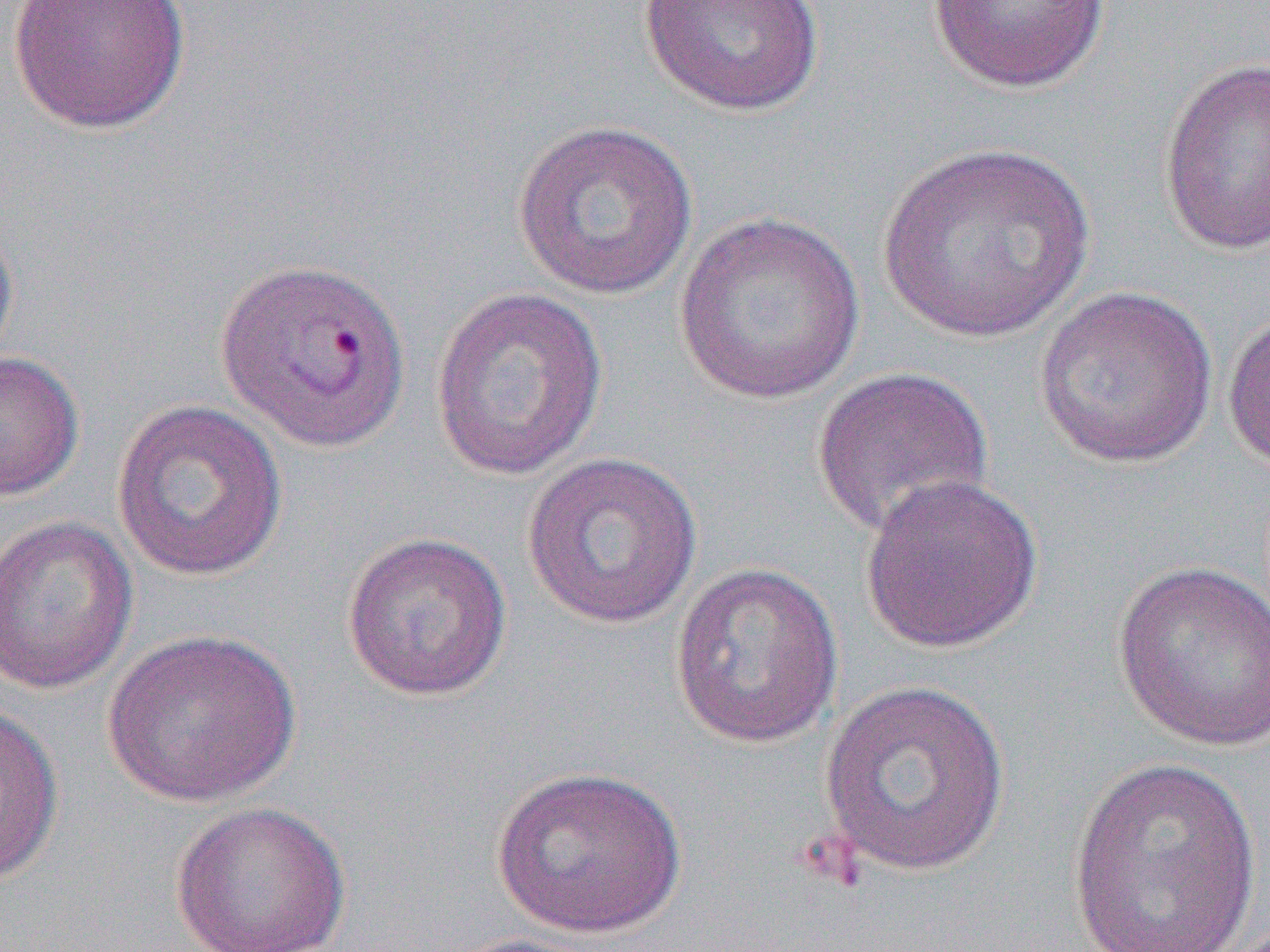

slide-level diagnosis = Plasmodium vivax
modality = light microscopy
magnification = 1000x
field of view = single
uninfected red blood cell locations = approximate bounding boxes as (x1, y1, x2, y2) in pixels: (7, 0, 192, 136), (638, 0, 827, 116), (927, 0, 1110, 95), (1158, 56, 1270, 258), (511, 119, 700, 301), (876, 142, 1097, 345), (673, 211, 867, 405), (0, 212, 20, 370), (1033, 284, 1220, 470), (429, 286, 609, 481), (1222, 305, 1270, 478), (0, 350, 85, 502), (810, 366, 995, 540), (111, 398, 288, 582), (520, 451, 705, 630), (859, 472, 1044, 654), (0, 515, 139, 696), (340, 530, 513, 701), (1110, 560, 1270, 753), (669, 561, 844, 749), (101, 628, 301, 807), (818, 679, 1012, 877), (0, 704, 65, 886), (1066, 755, 1265, 950), (490, 766, 689, 939), (169, 800, 352, 951), (442, 931, 611, 952)
image size = 1270×952 pixels
preparation = thin blood smear